Identify the parasite.
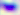
Toxoplasma gondii.

Summary:
  - Modality: photomicrograph
  - Magnification: 400x